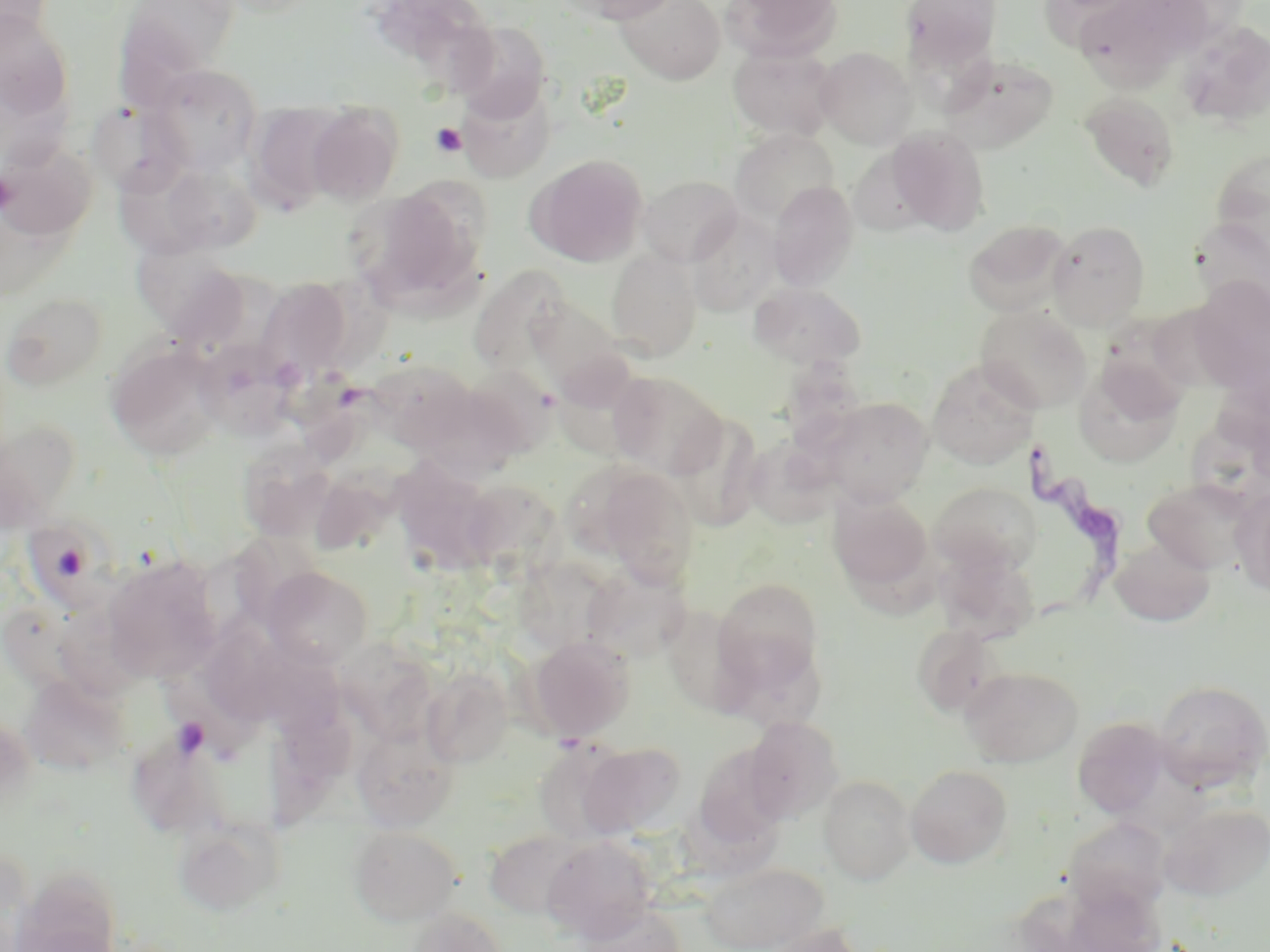
slide-level diagnosis = Trypanosoma brucei
field of view = one of a larger specimen
modality = light microscopy
image size = 1270×952 pixels
magnification = 1000x
platelet locations = approximate bounding boxes as (x1,y1)-(x2,y2) corner pairs in pixels: (430,123)-(467,157), (0,170)-(16,214), (170,716)-(211,759)
uninfected red blood cell locations = approximate bounding boxes as (x1,y1)-(x2,y2) corner pairs in pixels: (0,0)-(54,46), (115,0)-(241,100), (369,0)-(497,87), (565,0)-(683,24), (617,0)-(725,84), (723,0)-(843,61), (899,0)-(1003,75), (1077,0)-(1208,86), (0,10)-(75,122), (1175,20)-(1270,129), (449,21)-(552,121), (728,44)-(837,140), (815,47)-(917,148), (940,53)-(1059,152), (149,65)-(262,174), (456,80)-(553,184), (1080,91)-(1181,192), (86,98)-(191,198), (247,103)-(349,212), (306,104)-(403,206), (886,126)-(990,235), (731,128)-(840,226), (1,140)-(97,241), (528,154)-(648,267), (1210,154)-(1270,275), (120,156)-(226,259), (638,175)-(743,267), (768,181)-(860,291), (348,189)-(481,309), (686,208)-(781,315), (1192,217)-(1269,315), (963,219)-(1071,316), (1047,220)-(1150,329), (133,243)-(251,335), (606,249)-(702,361), (468,265)-(570,377), (254,277)-(355,382), (1190,278)-(1270,387), (749,283)-(866,369), (2,292)-(108,392), (525,296)-(628,395), (975,305)-(1091,413), (1104,307)-(1199,433), (193,338)-(299,438), (105,341)-(226,461), (366,358)-(478,450), (928,358)-(1039,469), (1079,359)-(1183,470), (461,364)-(558,459), (289,367)-(389,476), (608,372)-(726,479), (415,382)-(529,481), (818,397)-(932,506), (667,411)-(764,532), (1188,416)-(1270,510), (0,420)-(82,528), (744,436)-(837,530), (237,441)-(336,542), (392,451)-(512,576), (593,467)-(700,586), (1142,477)-(1259,575), (930,482)-(1041,575), (1231,488)-(1270,597), (830,493)-(933,596), (22,511)-(130,613), (1110,538)-(1214,628), (937,549)-(1039,642), (102,554)-(223,682), (582,563)-(692,660), (262,566)-(373,669), (714,578)-(823,686), (656,602)-(767,714), (48,607)-(148,717), (911,623)-(1003,717), (192,625)-(302,717), (528,635)-(636,741), (259,639)-(355,746), (733,640)-(833,732), (960,666)-(1083,767), (423,668)-(512,768), (21,672)-(128,775), (1152,679)-(1270,793), (291,682)-(380,783), (0,713)-(37,811), (742,716)-(843,822), (1072,716)-(1172,817), (352,724)-(459,831), (532,739)-(634,845), (577,741)-(687,838), (905,765)-(1013,868), (818,775)-(916,885), (1159,802)-(1270,900), (1063,816)-(1172,916), (172,817)-(280,917), (350,825)-(461,926), (484,830)-(589,920), (542,837)-(656,940), (16,855)-(125,949), (699,862)-(829,952), (1050,882)-(1168,952), (572,901)-(688,952), (404,908)-(506,952), (763,923)-(867,952)
preparation = thin blood film
stain = May-Grünwald-Giemsa
Trypanosoma brucei locations = approximate bounding boxes as (x1,y1)-(x2,y2) corner pairs in pixels: (1019,444)-(1131,640)